Draw a bounding box around every leukocyte (white blood cell).
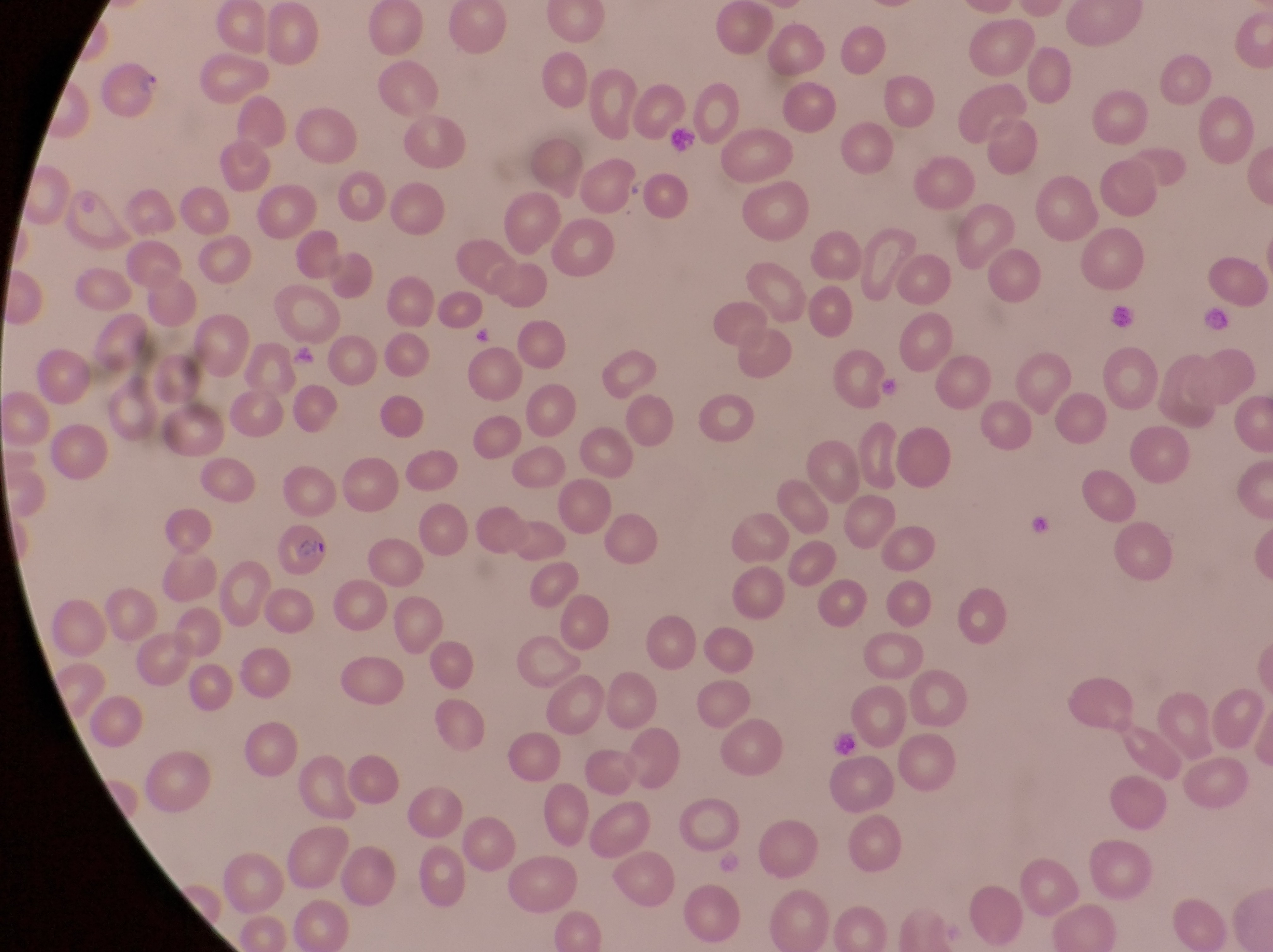

No leukocytes observed.

Approximate bounding boxes as [left, top, right, bottom] in pixels.
Summary:
  - Artifact (platelet-like body, stain precipitate, or debris) locations: [664, 122, 704, 165], [1110, 299, 1136, 331], [1203, 304, 1234, 338], [292, 345, 318, 371], [879, 372, 900, 398], [1031, 512, 1064, 549], [826, 727, 871, 770]
  - Parasitised red blood cell locations: [267, 527, 330, 579]
  - Magnification: 1000x
  - Image size: 1273×952 pixels
  - Field of view: single
  - Country: Uganda
  - Capture: smartphone photograph through the eyepiece of an Olympus CX-23 microscope
  - Preparation: thin blood smear